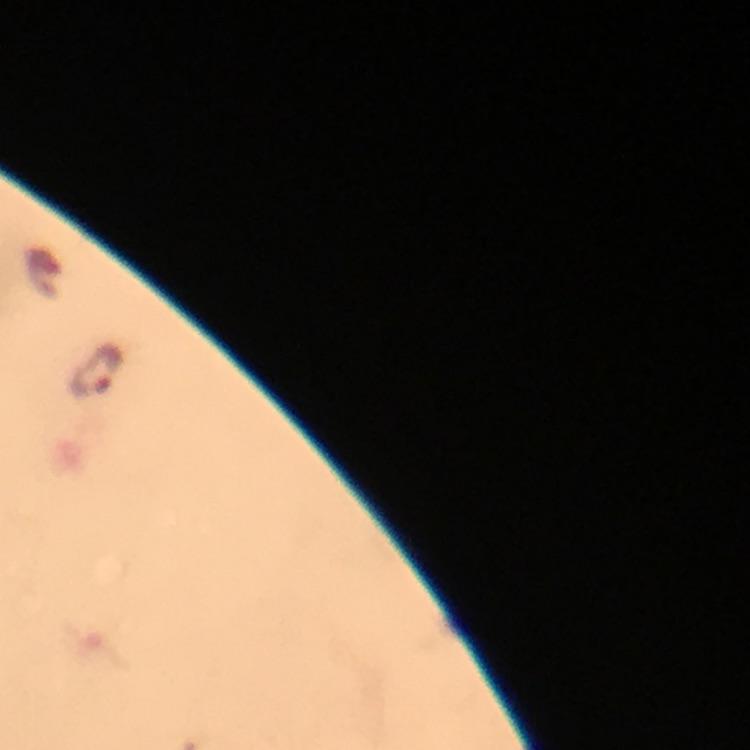
Approximate centers as (x, y) in pixels.
Summary:
  - Plasmodium parasite locations: (95, 371)
  - Immersion oil: applied
  - Stain: Giemsa
  - Context: from a diagnostic examination for malaria
  - Cropped from: one field of view
  - Magnification: 100x
  - Image size: 750×750 pixels
  - Preparation: thick blood smear
  - Capture: smartphone photograph through a microscope